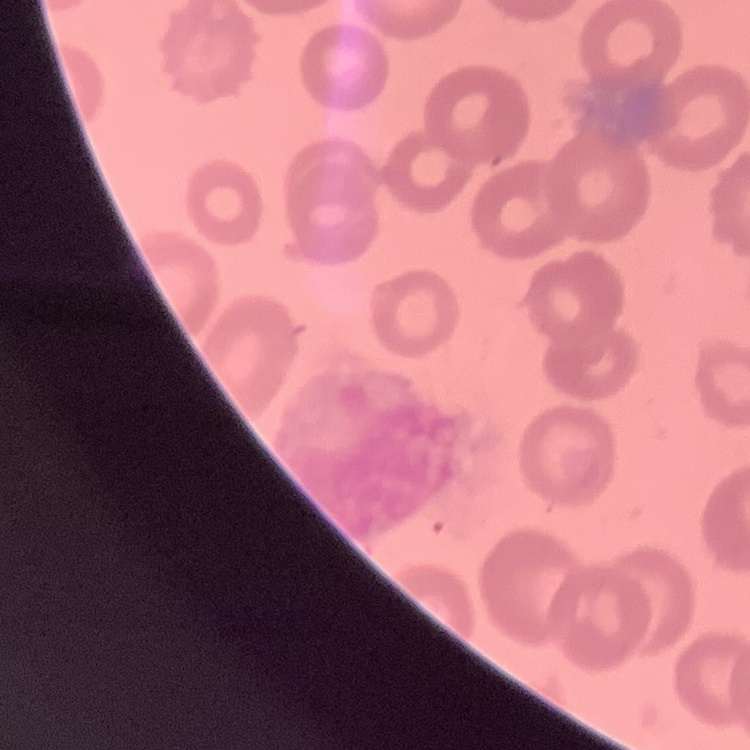

The red blood cells exhibit no rouleaux formation. Field's or Giemsa stain. One tile cut from a larger photomicrograph. Thin peripheral smear.